Locate every blood parasite and identify its species.
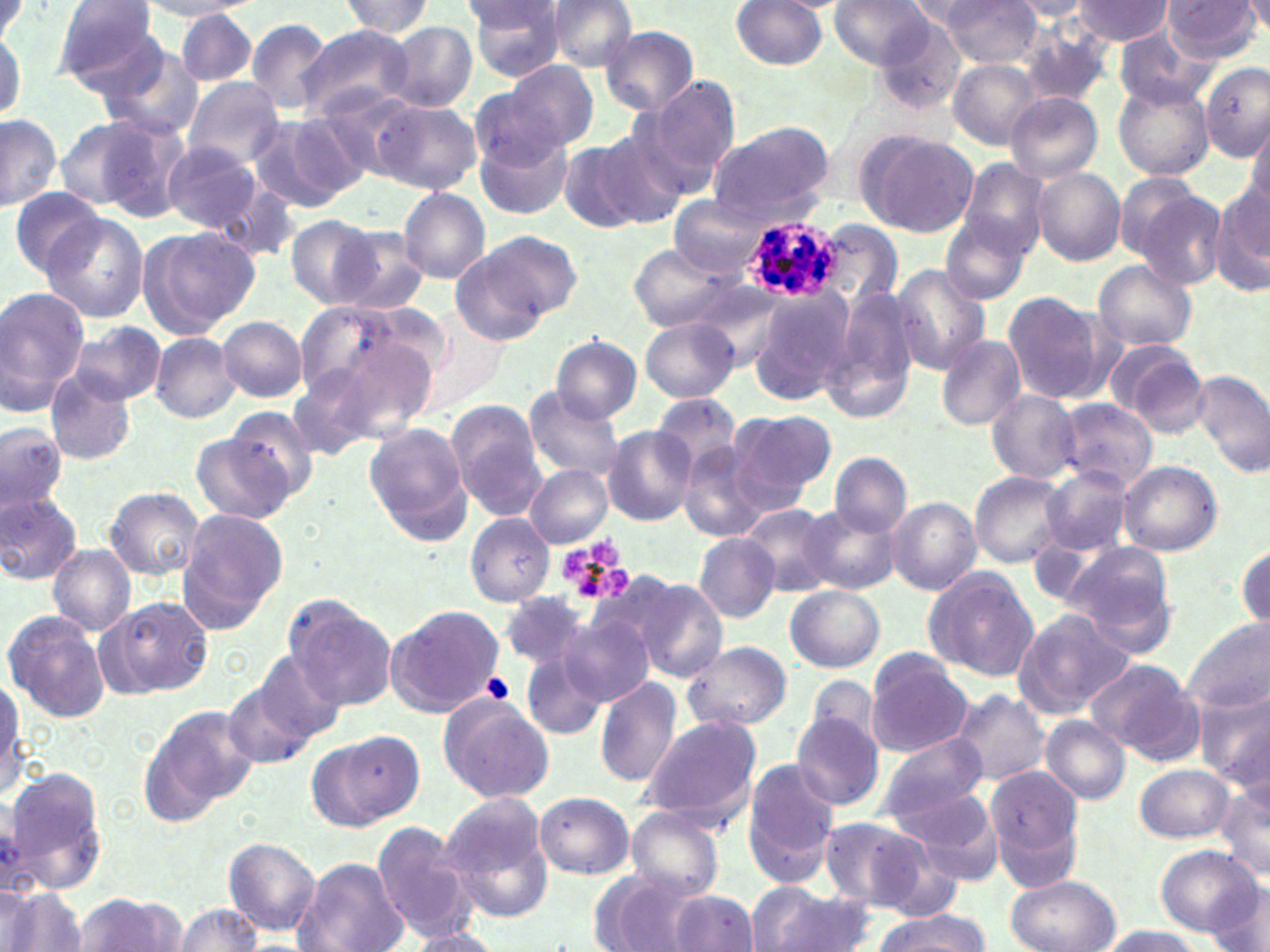
Approximate bounding boxes as (x1, y1, x2, y2) in pixels.
Plasmodium ovale-infected red blood cells: (742, 218, 843, 303).
No Plasmodium falciparum, Plasmodium malariae, Plasmodium vivax, Babesia divergens, or Trypanosoma brucei observed.

Summary:
  - Platelet locations: (558, 541, 632, 606), (479, 672, 514, 705)
  - Uninfected red blood cell locations: (0, 0, 26, 48), (52, 0, 162, 89), (463, 0, 570, 80), (544, 0, 638, 72), (829, 0, 934, 70), (939, 0, 1042, 67), (1163, 0, 1262, 63), (1246, 0, 1270, 38), (137, 1, 257, 20), (338, 1, 436, 38), (730, 1, 829, 71), (1072, 1, 1174, 45), (1007, 2, 1094, 21), (177, 8, 257, 87), (247, 17, 337, 115), (384, 22, 476, 112), (0, 23, 24, 126), (295, 24, 418, 125), (600, 26, 699, 115), (1019, 28, 1113, 111), (1113, 28, 1211, 112), (99, 45, 203, 140), (503, 60, 599, 153), (948, 60, 1043, 149), (1200, 62, 1270, 160), (181, 76, 285, 168), (645, 77, 741, 182), (1114, 80, 1214, 181), (1006, 92, 1103, 182), (368, 98, 481, 195), (247, 113, 362, 214), (83, 114, 191, 222), (0, 116, 61, 211), (51, 117, 154, 210), (1244, 119, 1270, 218), (595, 122, 697, 226), (706, 123, 836, 228), (474, 126, 574, 221), (862, 132, 979, 237), (559, 140, 649, 234), (162, 141, 262, 234), (956, 157, 1050, 259), (1031, 167, 1125, 265), (1121, 180, 1227, 291), (1210, 183, 1270, 298), (9, 186, 106, 279), (399, 187, 490, 282), (670, 198, 764, 277), (43, 214, 150, 322), (285, 216, 381, 309), (816, 217, 903, 310), (940, 217, 1031, 304), (141, 226, 259, 334), (332, 227, 431, 315), (475, 230, 583, 326), (627, 244, 733, 332), (453, 247, 555, 345), (1093, 260, 1196, 352), (890, 264, 990, 373), (749, 286, 857, 407), (827, 286, 923, 420), (0, 288, 89, 416), (1002, 291, 1112, 404), (217, 316, 307, 401), (641, 317, 739, 402), (69, 322, 165, 404), (150, 331, 241, 423), (936, 334, 1025, 431), (317, 335, 437, 441), (550, 336, 641, 423), (1106, 341, 1209, 438), (1193, 369, 1270, 477), (46, 372, 135, 465), (523, 388, 627, 482), (985, 390, 1081, 485), (651, 395, 738, 475), (1054, 399, 1157, 492), (449, 404, 545, 522), (221, 407, 319, 507), (726, 409, 834, 513), (0, 421, 67, 518), (362, 422, 473, 546), (602, 428, 698, 526), (191, 433, 294, 525), (678, 444, 768, 541), (830, 452, 910, 536), (1117, 460, 1222, 556), (525, 465, 613, 547), (1041, 468, 1133, 557), (969, 471, 1070, 567), (104, 487, 204, 579), (0, 490, 82, 584), (886, 498, 980, 594), (799, 501, 900, 596), (740, 503, 835, 596), (176, 508, 289, 628), (465, 515, 554, 606), (695, 533, 780, 622), (1065, 540, 1179, 654), (1235, 541, 1268, 633), (47, 544, 135, 636), (923, 566, 1038, 681), (636, 577, 728, 681), (785, 585, 885, 672), (499, 591, 592, 670), (97, 595, 214, 699), (284, 597, 393, 711), (386, 605, 504, 716), (1012, 609, 1137, 719), (3, 610, 109, 721), (562, 615, 656, 710), (1182, 620, 1269, 714), (682, 641, 791, 731), (249, 650, 349, 744), (865, 651, 974, 756), (521, 652, 606, 739), (1084, 659, 1202, 761), (803, 674, 884, 760), (0, 675, 27, 795), (594, 676, 682, 789), (223, 677, 317, 769), (1198, 687, 1270, 792), (950, 689, 1051, 786), (439, 696, 554, 803), (139, 708, 251, 828), (790, 712, 885, 812), (639, 714, 762, 829), (1040, 715, 1131, 804), (337, 728, 423, 825), (872, 734, 990, 825), (743, 759, 838, 877), (1135, 763, 1236, 844), (5, 766, 109, 893), (986, 769, 1082, 883), (1216, 781, 1270, 881), (892, 785, 1006, 880), (533, 791, 634, 879), (440, 798, 555, 922), (624, 805, 725, 902), (817, 817, 931, 911), (371, 820, 474, 939), (222, 838, 321, 936), (1151, 845, 1260, 938), (291, 858, 408, 952), (592, 872, 705, 951), (1206, 873, 1270, 952), (1005, 875, 1120, 952), (748, 883, 870, 952), (3, 890, 88, 952), (668, 891, 759, 952), (74, 893, 184, 952), (174, 901, 261, 952), (867, 913, 990, 950), (1092, 924, 1203, 951), (402, 931, 507, 952)
  - Slide-level diagnosis: Plasmodium ovale
  - Preparation: thin blood film
  - Modality: light microscopy
  - Field of view: single
  - Magnification: 1000x
  - Image size: 1270×952 pixels
  - Stain: May-Grünwald-Giemsa